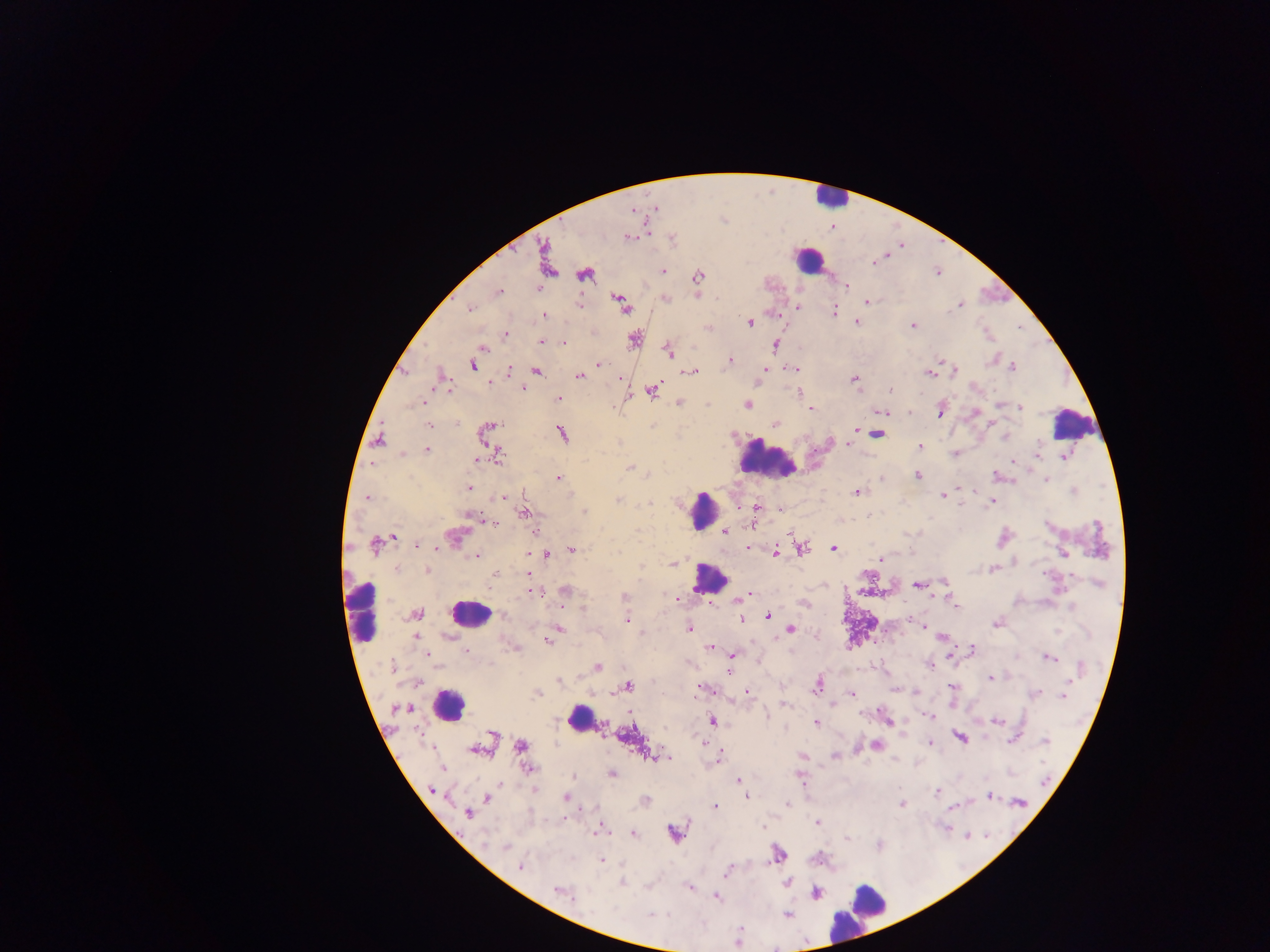 Approximate centers as (x, y) in pixels. Leukocyte locations: (828, 196), (807, 260), (1074, 423), (766, 459), (704, 510), (709, 578), (361, 611), (469, 614), (448, 705), (580, 719), (859, 911). Plasmodium parasite locations: (632, 212), (629, 238), (546, 253), (874, 262), (663, 271), (584, 275), (698, 276), (847, 286), (498, 291), (867, 302), (622, 304), (960, 305), (579, 306), (798, 307), (470, 309), (834, 312), (545, 315), (857, 321), (749, 322), (913, 326), (707, 328), (507, 335), (634, 340), (541, 342), (563, 342), (776, 345), (483, 348), (668, 351), (942, 360), (730, 361), (600, 364), (473, 366), (1012, 367), (509, 369), (794, 369), (765, 370), (537, 371), (691, 371), (955, 371), (930, 373), (580, 376), (618, 379), (855, 380), (490, 382), (523, 388), (891, 389), (652, 391), (798, 394), (558, 399), (424, 402), (679, 402), (1000, 404), (747, 405), (1020, 407), (810, 409), (882, 412), (909, 412), (940, 412), (974, 412), (490, 424), (775, 424), (429, 426), (487, 430), (854, 430), (562, 434), (877, 434), (1004, 437), (380, 439), (847, 444), (920, 447), (426, 450), (402, 453), (955, 453), (499, 455), (1064, 456), (476, 460), (1013, 461), (629, 468), (918, 476), (996, 476), (557, 477), (883, 479), (1046, 479), (469, 488), (972, 491), (857, 492), (942, 495), (503, 497), (366, 498), (618, 500), (649, 503), (992, 503), (757, 507), (781, 509), (585, 512), (524, 514), (869, 514), (471, 515), (488, 521), (752, 525), (724, 531), (456, 536), (393, 537), (375, 545), (417, 545), (436, 547), (749, 548), (801, 548), (571, 549), (834, 549), (775, 552), (1063, 553), (546, 555), (476, 556), (880, 558), (673, 564), (395, 569), (993, 570), (427, 571), (495, 574), (528, 574), (918, 584), (1100, 585), (532, 591), (565, 592), (625, 596), (743, 597), (677, 598), (956, 606), (1071, 606), (561, 607), (583, 609), (416, 614), (502, 614), (769, 616), (741, 619), (626, 620), (996, 623), (923, 627), (559, 628), (688, 628), (791, 629), (553, 633), (642, 633), (447, 636), (416, 638), (941, 638), (547, 641), (711, 648), (972, 650), (466, 652), (427, 654), (733, 654), (950, 657), (1048, 657), (391, 666), (598, 666), (931, 666), (729, 672), (991, 678), (558, 681), (627, 686), (817, 686), (953, 686), (702, 689), (747, 693), (916, 693), (1036, 693), (537, 694), (852, 694), (1063, 695), (784, 704), (766, 715), (929, 716), (887, 719), (712, 721), (997, 722), (816, 723), (492, 734), (961, 737), (1014, 739), (701, 741), (1045, 741), (930, 743), (521, 745), (875, 745), (475, 750), (834, 756), (653, 758), (664, 759), (718, 759), (443, 768), (529, 768), (611, 774), (573, 776), (801, 776), (739, 780), (1046, 782), (741, 785), (431, 790), (937, 791), (747, 796), (989, 796), (566, 797), (486, 798), (645, 800), (1019, 802), (787, 803), (902, 804), (715, 807), (467, 813), (817, 822), (762, 827), (599, 830), (674, 832), (633, 833), (966, 835), (847, 839), (485, 843), (879, 845), (505, 847), (777, 854), (602, 861), (520, 865), (729, 871), (787, 882), (622, 883), (690, 888), (557, 890), (815, 894), (716, 897), (652, 914), (787, 915). Collected in Ghana. Single field of view. Thick blood film. Photographed through a microscope with a mobile-phone camera. Image is 1270×952 pixels.